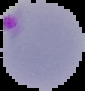

Summary:
  - Image type: segmented cell region with the area outside set to black
  - Preparation: thin blood smear
  - Malaria status: parasitized
  - Image size: 85×91 pixels